Name the cell type shown.
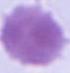

This is an erythrocyte.

Photomicrograph. 1000x magnification.